Give the extent of all Plasmodium falciparum-infected red blood cells.
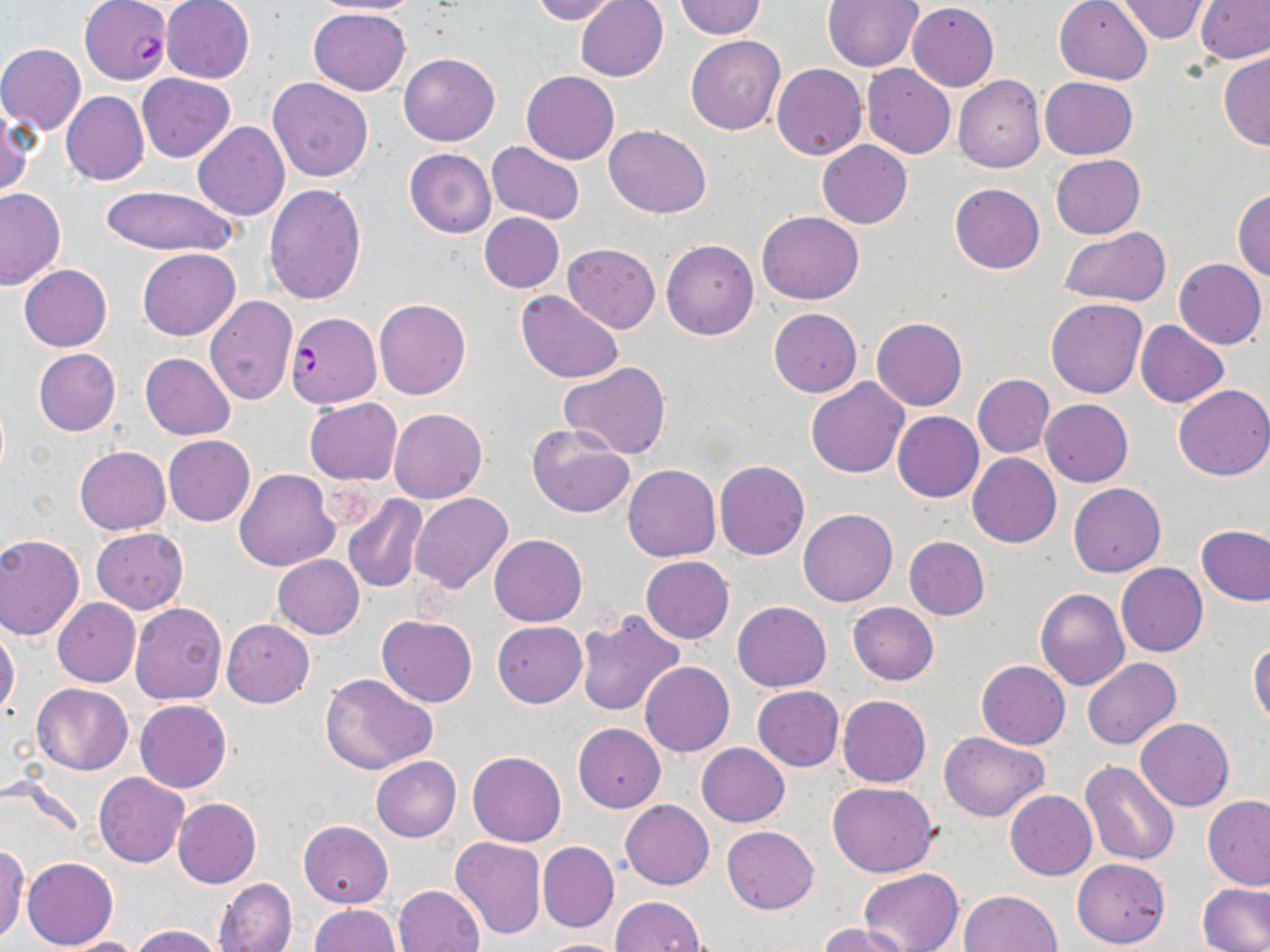
Approximate bounding boxes as (x1, y1, x2, y2) in pixels.
Plasmodium falciparum-infected red blood cells: (79, 1, 171, 86), (285, 311, 381, 407).

Summary:
  - Uninfected red blood cell locations: (305, 0, 423, 15), (530, 0, 622, 24), (574, 0, 668, 82), (1115, 0, 1210, 42), (162, 1, 255, 83), (673, 1, 766, 39), (821, 1, 925, 72), (1054, 1, 1154, 84), (1196, 1, 1270, 64), (907, 3, 999, 91), (309, 7, 410, 95), (685, 35, 785, 134), (1, 43, 86, 134), (1219, 50, 1270, 150), (399, 52, 500, 146), (772, 63, 867, 161), (862, 64, 954, 159), (521, 70, 619, 164), (138, 74, 234, 161), (952, 75, 1045, 173), (268, 77, 373, 181), (1040, 77, 1137, 160), (61, 91, 149, 186), (0, 105, 33, 197), (193, 122, 289, 221), (604, 124, 711, 217), (817, 140, 912, 228), (486, 141, 584, 226), (404, 148, 496, 239), (1051, 155, 1145, 238), (263, 183, 365, 305), (949, 183, 1044, 274), (98, 185, 237, 256), (0, 188, 65, 290), (1232, 188, 1270, 280), (758, 210, 863, 304), (479, 212, 564, 292), (1059, 226, 1172, 307), (661, 239, 758, 340), (562, 242, 660, 333), (137, 248, 240, 340), (1174, 258, 1267, 348), (19, 264, 113, 351), (515, 291, 623, 383), (203, 295, 297, 404), (373, 298, 471, 400), (1045, 298, 1147, 398), (769, 308, 861, 398), (871, 317, 966, 411), (1135, 320, 1227, 407), (33, 348, 120, 436), (140, 352, 235, 439), (559, 362, 670, 457), (973, 374, 1053, 458), (806, 378, 908, 478), (974, 384, 1129, 468), (1172, 384, 1270, 480), (304, 398, 402, 485), (1040, 398, 1133, 486), (389, 407, 488, 504), (892, 411, 984, 503), (526, 424, 634, 519), (163, 435, 255, 526), (75, 445, 171, 535), (967, 453, 1061, 548), (714, 460, 809, 560), (623, 463, 720, 562), (235, 469, 340, 571), (1068, 483, 1165, 577), (343, 493, 428, 593), (410, 493, 513, 594), (799, 508, 898, 607), (1196, 525, 1270, 606), (91, 528, 188, 613), (0, 533, 85, 639), (489, 534, 586, 626), (903, 535, 990, 620), (273, 555, 364, 639), (640, 555, 733, 643), (1116, 562, 1208, 656), (1036, 587, 1130, 690), (52, 599, 140, 686), (732, 601, 832, 692), (847, 602, 939, 685), (130, 603, 228, 706), (573, 609, 685, 717), (377, 615, 476, 708), (221, 620, 313, 707), (492, 621, 587, 706), (0, 626, 20, 721), (1248, 638, 1270, 730), (1082, 657, 1181, 749), (976, 660, 1069, 749), (639, 661, 734, 756), (320, 673, 437, 776), (32, 683, 132, 775), (752, 685, 844, 771), (838, 695, 931, 787), (135, 698, 232, 792), (1135, 718, 1235, 812), (573, 723, 665, 812), (938, 731, 1048, 821), (696, 743, 789, 827), (468, 751, 566, 846), (371, 755, 461, 842), (1079, 761, 1180, 866), (94, 774, 188, 867), (828, 782, 938, 878), (1005, 790, 1096, 880), (1203, 795, 1270, 891), (172, 797, 261, 889), (621, 800, 714, 889), (298, 820, 393, 909), (722, 826, 819, 914), (451, 837, 546, 940), (538, 842, 618, 932), (0, 846, 29, 942), (21, 857, 118, 949), (1071, 857, 1170, 949), (858, 868, 964, 952), (215, 878, 296, 952), (1197, 882, 1270, 952), (393, 885, 484, 952), (959, 891, 1062, 952), (611, 896, 707, 952), (310, 904, 400, 952), (818, 923, 913, 952), (130, 925, 226, 952), (56, 937, 146, 952), (532, 938, 630, 952)
  - Slide-level diagnosis: Plasmodium falciparum
  - Magnification: 1000x
  - Stain: May-Grünwald-Giemsa
  - Modality: optical microscopy
  - Preparation: thin blood film
  - Field of view: one of a larger specimen
  - Image size: 1270×952 pixels